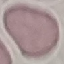

Summary:
  - Malaria status: uninfected
  - Stain: Giemsa
  - Image type: automatically extracted cell patch, resized to 64 × 64 pixels
  - Preparation: thin blood film
  - Capture: smartphone through the microscope eyepiece